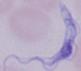
Summary:
  - Identification: trypanosome
  - Modality: micrograph
  - Magnification: 1000x